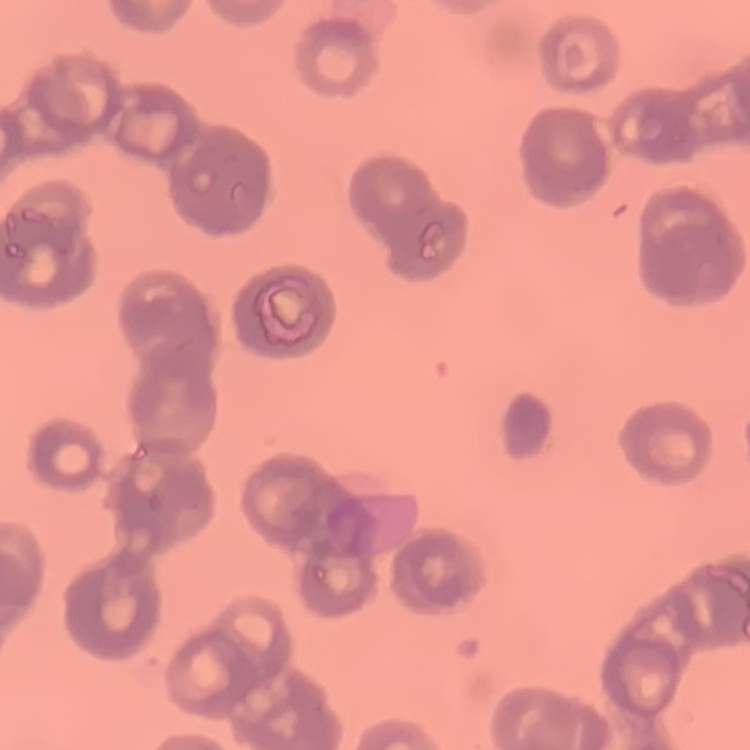
Summary:
  - Red blood cell morphology: rouleaux formation
  - Preparation: thin blood smear
  - Image type: square crop of a larger photomicrograph
  - Stain: Field's or Giemsa